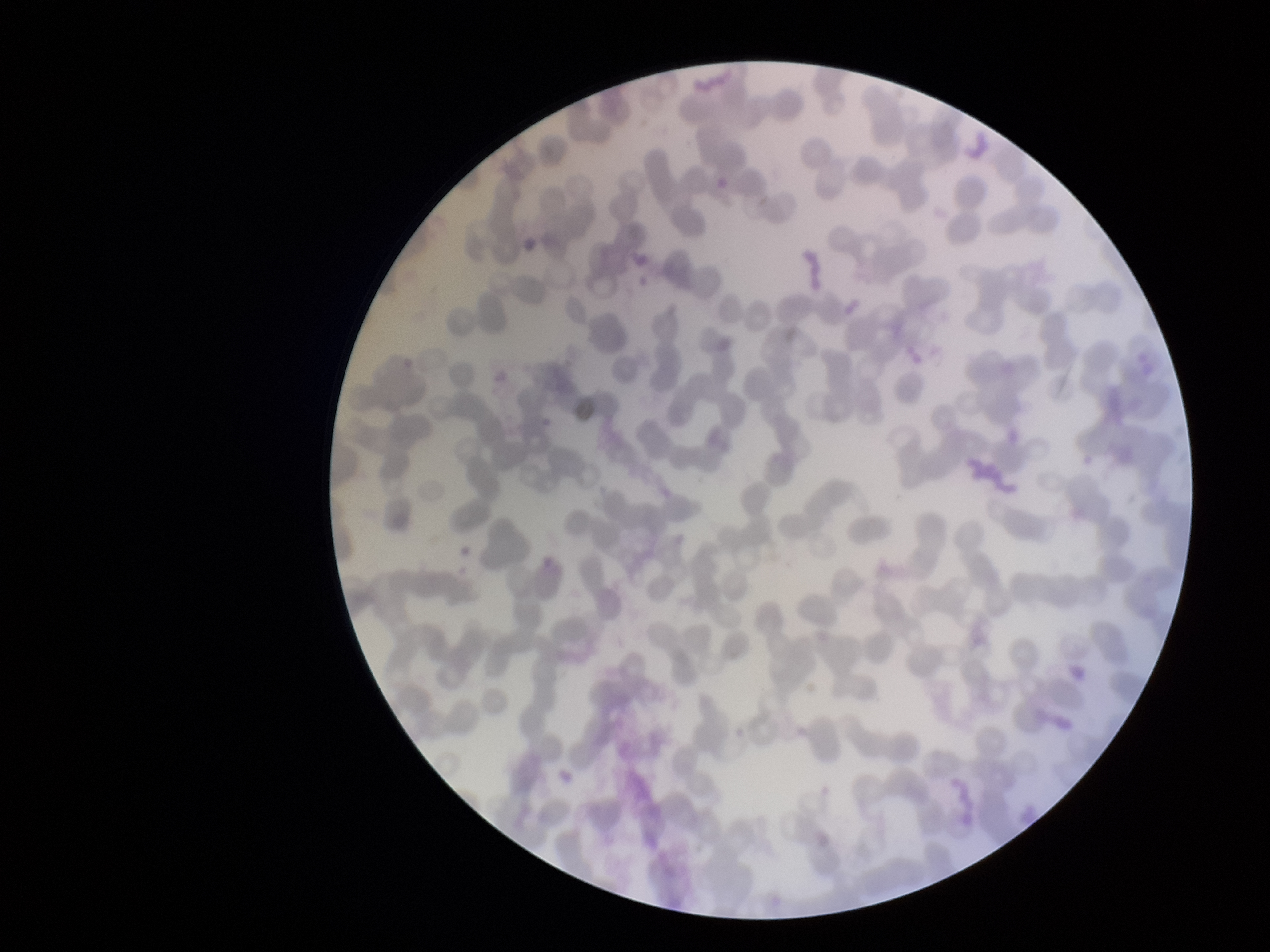
field of view = one from this slide
red blood cell count = 264
preparation = thin smear
patient malaria status = negative
image size = 1270×952 pixels
stain = Giemsa
parasitized red blood cell count = 0
parasitized red blood cells = none seen
capture = smartphone photograph through the microscope eyepiece